Classify this cell by malaria status.
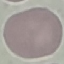
Uninfected.

preparation = thin smear
capture = smartphone camera at the microscope eyepiece
stain = Giemsa
image type = automatically extracted cell patch, resized to 64 × 64 pixels